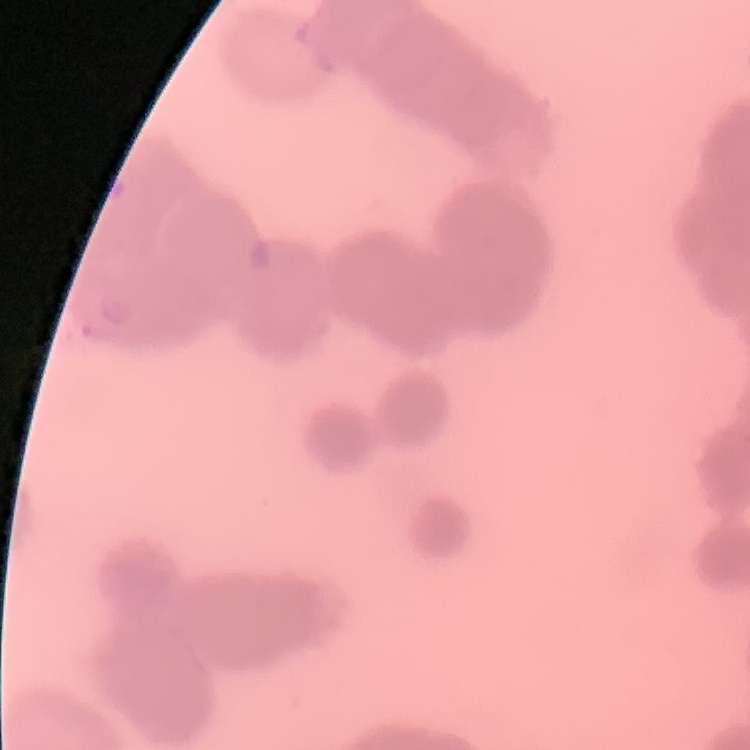
{
  "erythrocyte_morphology": "rouleaux formation",
  "image_type": "one tile cut from a larger photomicrograph",
  "preparation": "thin blood film",
  "stain": "Field's or Giemsa"
}